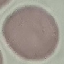

malaria_status: uninfected
capture: smartphone through the microscope eyepiece
stain: Giemsa
image_type: cell patch, automatically extracted from a larger field of view and resized to 64 × 64 pixels
preparation: thin blood film